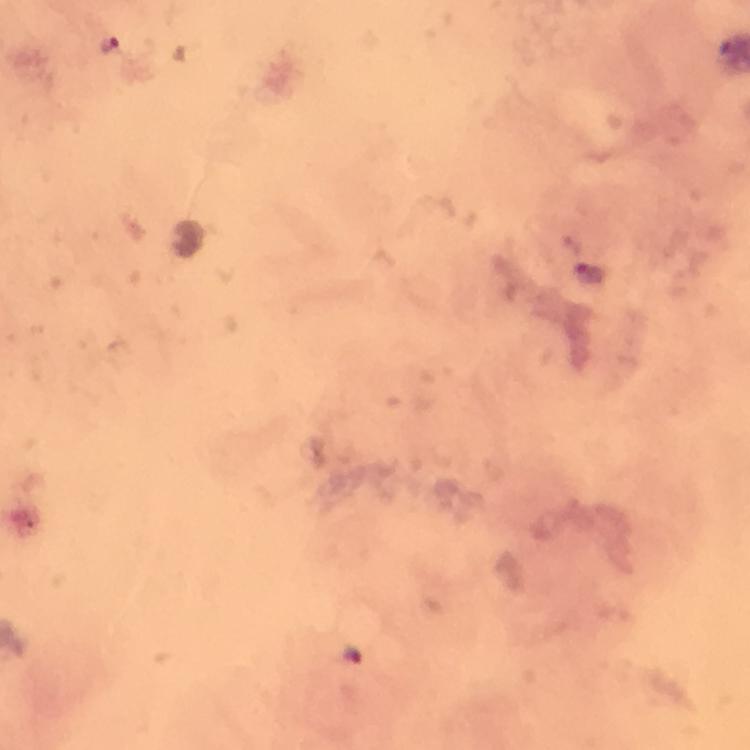
Approximate centers as {x, y} in pixels.
Summary:
  - Plasmodium parasite locations: {110, 45}, {589, 274}, {352, 654}
  - Preparation: thick blood film
  - Capture: smartphone camera through the microscope
  - Stain: Giemsa
  - Cropped from: one field of view
  - Image size: 750×750 pixels
  - Immersion oil: applied
  - Magnification: 100x
  - Context: from a diagnostic examination for malaria